Locate every malaria parasite.
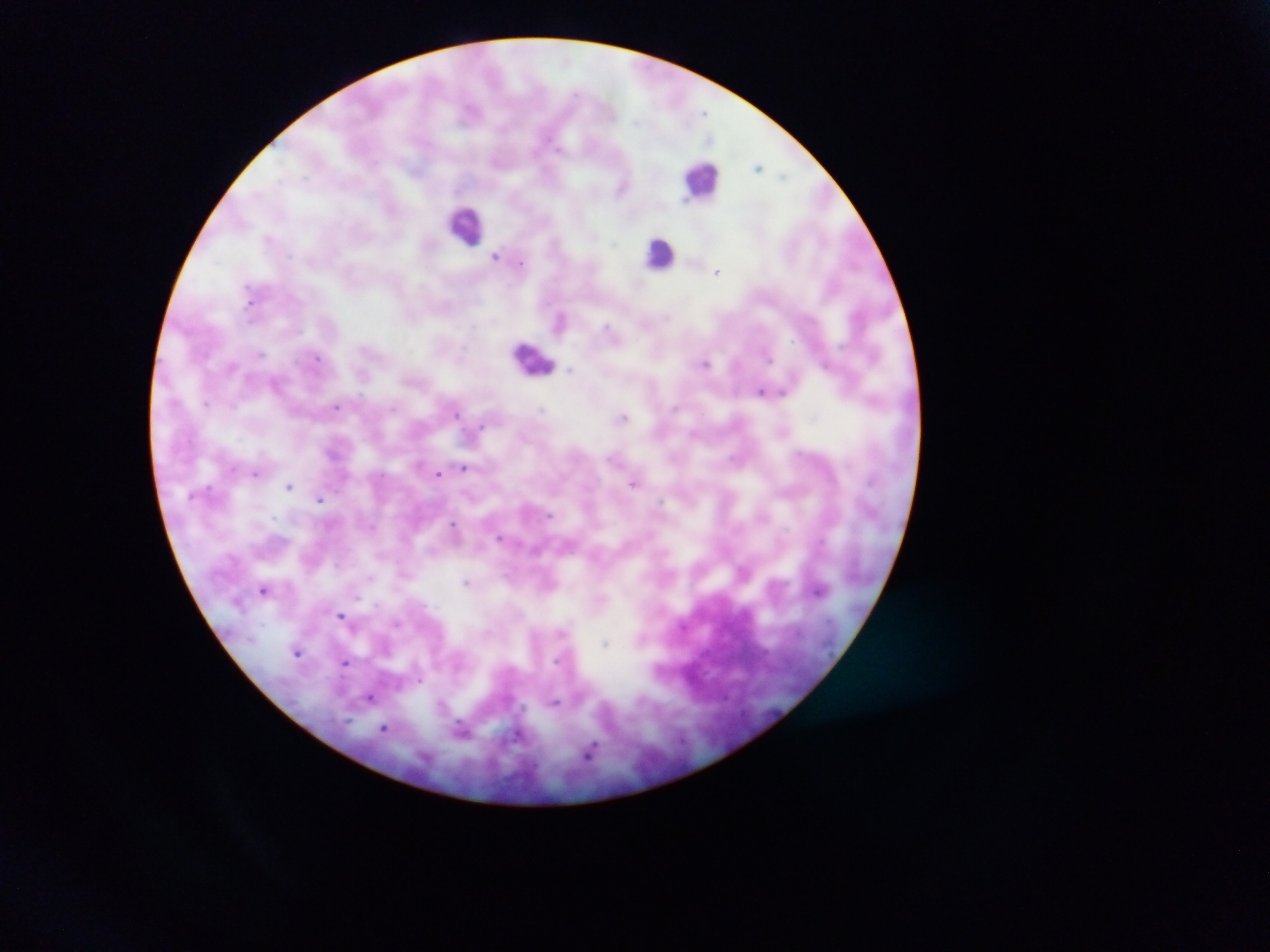
Approximate centers as {x, y} in pixels.
Malaria parasites: {705, 112}, {709, 139}, {759, 167}, {781, 175}, {621, 187}, {267, 238}, {615, 244}, {495, 257}, {521, 265}, {717, 272}, {248, 301}, {666, 316}, {608, 326}, {791, 341}, {261, 353}, {317, 358}, {768, 358}, {705, 363}, {230, 367}, {570, 371}, {364, 376}, {761, 392}, {781, 392}, {206, 403}, {335, 407}, {675, 407}, {394, 408}, {541, 408}, {456, 414}, {623, 417}, {482, 425}, {694, 433}, {463, 468}, {255, 473}, {438, 473}, {633, 483}, {289, 486}, {319, 499}, {660, 501}, {549, 515}, {273, 517}, {453, 523}, {500, 537}, {370, 576}, {466, 582}, {264, 590}, {819, 591}, {357, 597}, {341, 615}, {396, 622}, {562, 632}, {604, 643}, {297, 653}, {344, 662}, {420, 680}, {370, 698}, {555, 702}, {384, 727}, {462, 729}, {518, 736}, {590, 752}.

Summary:
  - Leukocyte locations: {701, 177}, {466, 225}, {660, 253}, {535, 360}
  - Field of view: single
  - Country: Ghana
  - Preparation: thick blood film
  - Image size: 1270×952 pixels
  - Capture: mobile-phone photograph through a microscope